Name the cell type shown.
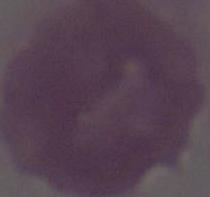
This is an erythrocyte.

Summary:
  - Magnification: 1000x
  - Modality: photomicrograph